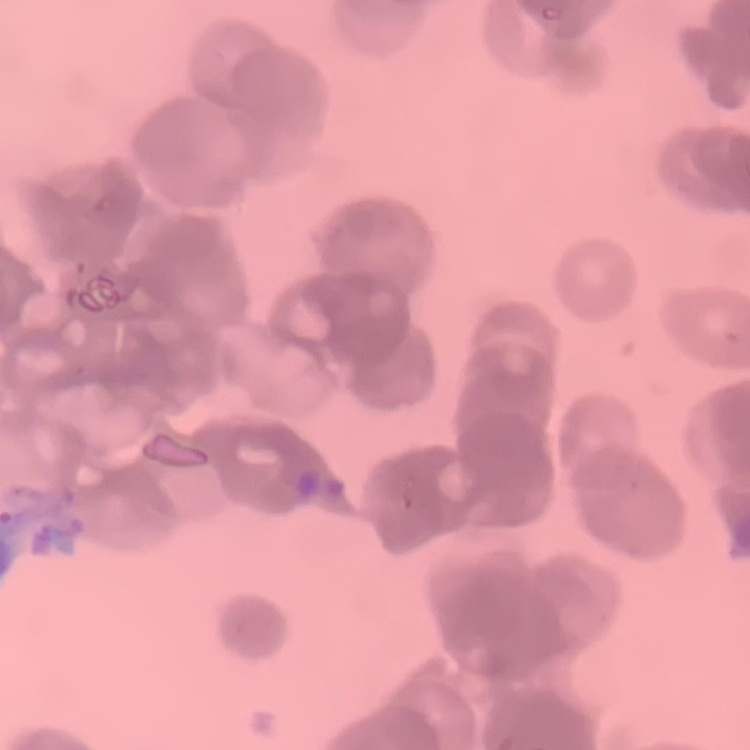
Summary:
  - Erythrocyte morphology: rouleaux formation
  - Image type: square crop of a larger photomicrograph
  - Stain: Field's or Giemsa
  - Preparation: thin blood film